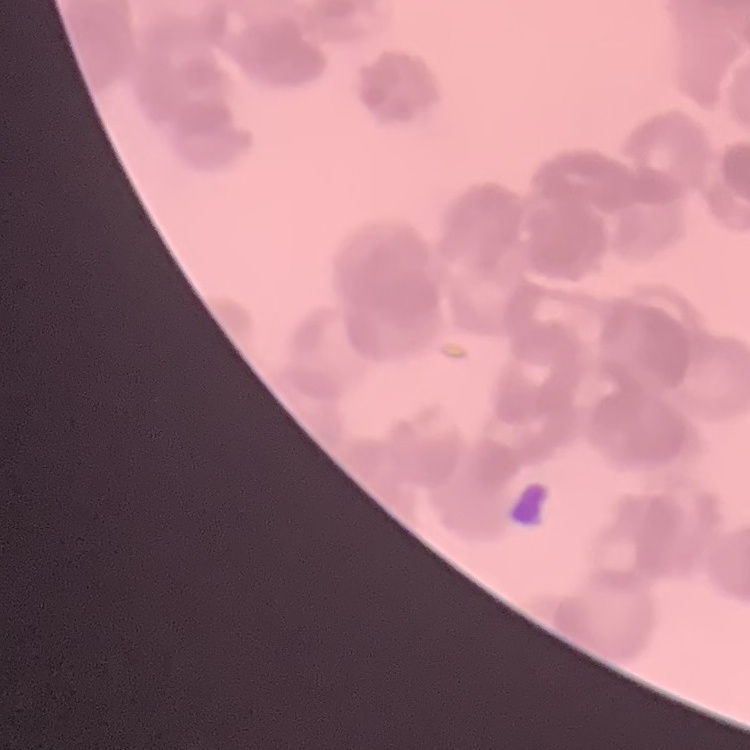

Summary:
  - Red blood cell morphology: rouleaux formation
  - Preparation: thin peripheral smear
  - Image type: square crop of a larger photomicrograph
  - Stain: Field's or Giemsa